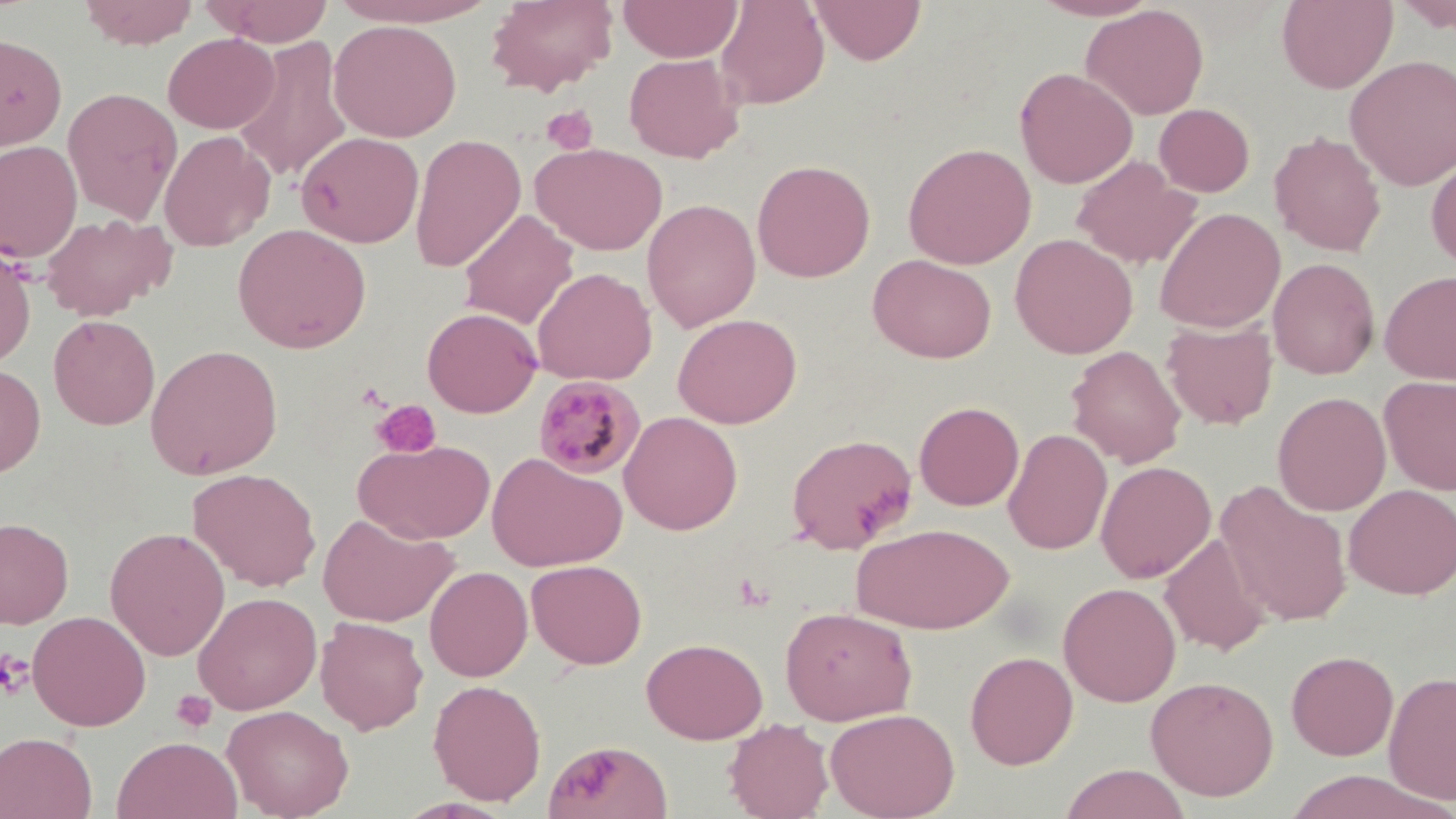

slide-level diagnosis = Plasmodium malariae
modality = light microscopy
field of view = one of a larger specimen
uninfected red blood cell locations = approximate bounding boxes as named x1/y1/x2/y2 corners in pixels: (x1=78, y1=0, x2=199, y2=49), (x1=207, y1=0, x2=334, y2=46), (x1=329, y1=0, x2=499, y2=27), (x1=486, y1=0, x2=618, y2=96), (x1=617, y1=0, x2=743, y2=63), (x1=715, y1=0, x2=829, y2=110), (x1=810, y1=0, x2=927, y2=65), (x1=1029, y1=0, x2=1161, y2=21), (x1=1276, y1=0, x2=1398, y2=93), (x1=1393, y1=0, x2=1456, y2=34), (x1=1082, y1=3, x2=1209, y2=120), (x1=328, y1=19, x2=462, y2=142), (x1=0, y1=32, x2=67, y2=150), (x1=163, y1=33, x2=279, y2=134), (x1=234, y1=35, x2=353, y2=184), (x1=624, y1=53, x2=745, y2=163), (x1=1345, y1=55, x2=1456, y2=191), (x1=1014, y1=67, x2=1138, y2=189), (x1=62, y1=87, x2=182, y2=225), (x1=1154, y1=103, x2=1255, y2=197), (x1=159, y1=130, x2=274, y2=251), (x1=296, y1=131, x2=424, y2=248), (x1=1269, y1=131, x2=1387, y2=257), (x1=409, y1=133, x2=527, y2=273), (x1=0, y1=140, x2=82, y2=264), (x1=532, y1=142, x2=668, y2=255), (x1=902, y1=142, x2=1036, y2=269), (x1=1070, y1=155, x2=1202, y2=269), (x1=1426, y1=155, x2=1456, y2=271), (x1=751, y1=159, x2=876, y2=282), (x1=642, y1=198, x2=761, y2=331), (x1=1155, y1=207, x2=1286, y2=334), (x1=458, y1=208, x2=578, y2=329), (x1=40, y1=212, x2=173, y2=321), (x1=233, y1=223, x2=371, y2=354), (x1=1009, y1=233, x2=1138, y2=359), (x1=0, y1=245, x2=37, y2=367), (x1=867, y1=253, x2=997, y2=363), (x1=1268, y1=258, x2=1380, y2=379), (x1=532, y1=266, x2=657, y2=384), (x1=1379, y1=270, x2=1456, y2=386), (x1=422, y1=307, x2=542, y2=417), (x1=673, y1=313, x2=802, y2=429), (x1=48, y1=314, x2=160, y2=430), (x1=1161, y1=320, x2=1278, y2=430), (x1=145, y1=344, x2=284, y2=480), (x1=1066, y1=345, x2=1186, y2=468), (x1=0, y1=362, x2=46, y2=478), (x1=1378, y1=374, x2=1456, y2=496), (x1=1272, y1=391, x2=1392, y2=516), (x1=914, y1=401, x2=1024, y2=510), (x1=619, y1=411, x2=743, y2=535), (x1=1003, y1=428, x2=1112, y2=555), (x1=785, y1=433, x2=918, y2=553), (x1=354, y1=439, x2=495, y2=544), (x1=487, y1=452, x2=627, y2=572), (x1=1095, y1=460, x2=1216, y2=583), (x1=188, y1=467, x2=322, y2=591), (x1=1215, y1=480, x2=1353, y2=627), (x1=1344, y1=484, x2=1456, y2=599), (x1=317, y1=513, x2=457, y2=627), (x1=0, y1=517, x2=74, y2=628), (x1=851, y1=522, x2=1015, y2=634), (x1=105, y1=526, x2=230, y2=661), (x1=1159, y1=534, x2=1273, y2=655), (x1=526, y1=559, x2=647, y2=670), (x1=424, y1=566, x2=533, y2=681), (x1=1058, y1=582, x2=1181, y2=707), (x1=193, y1=591, x2=322, y2=715), (x1=779, y1=606, x2=918, y2=725), (x1=27, y1=610, x2=151, y2=731), (x1=315, y1=616, x2=428, y2=734), (x1=641, y1=637, x2=768, y2=744), (x1=965, y1=650, x2=1079, y2=769), (x1=1286, y1=650, x2=1399, y2=760), (x1=1383, y1=669, x2=1456, y2=807), (x1=1145, y1=675, x2=1279, y2=800), (x1=428, y1=679, x2=546, y2=805), (x1=222, y1=703, x2=354, y2=819), (x1=824, y1=707, x2=960, y2=819), (x1=723, y1=717, x2=834, y2=819), (x1=0, y1=732, x2=97, y2=818), (x1=112, y1=735, x2=242, y2=819), (x1=543, y1=740, x2=673, y2=819), (x1=1059, y1=764, x2=1191, y2=819), (x1=1281, y1=770, x2=1445, y2=818)
platelet locations = approximate bounding boxes as named x1/y1/x2/y2 corners in pixels: (x1=541, y1=105, x2=599, y2=155), (x1=371, y1=399, x2=442, y2=458), (x1=0, y1=649, x2=34, y2=699), (x1=171, y1=689, x2=217, y2=733)
preparation = thin blood film
image size = 1456×819 pixels
stain = May-Grünwald-Giemsa
magnification = 1000x
Plasmodium malariae-infected red blood cell locations = approximate bounding boxes as named x1/y1/x2/y2 corners in pixels: (x1=533, y1=376, x2=647, y2=480)